Evaluate for Plasmodium parasites.
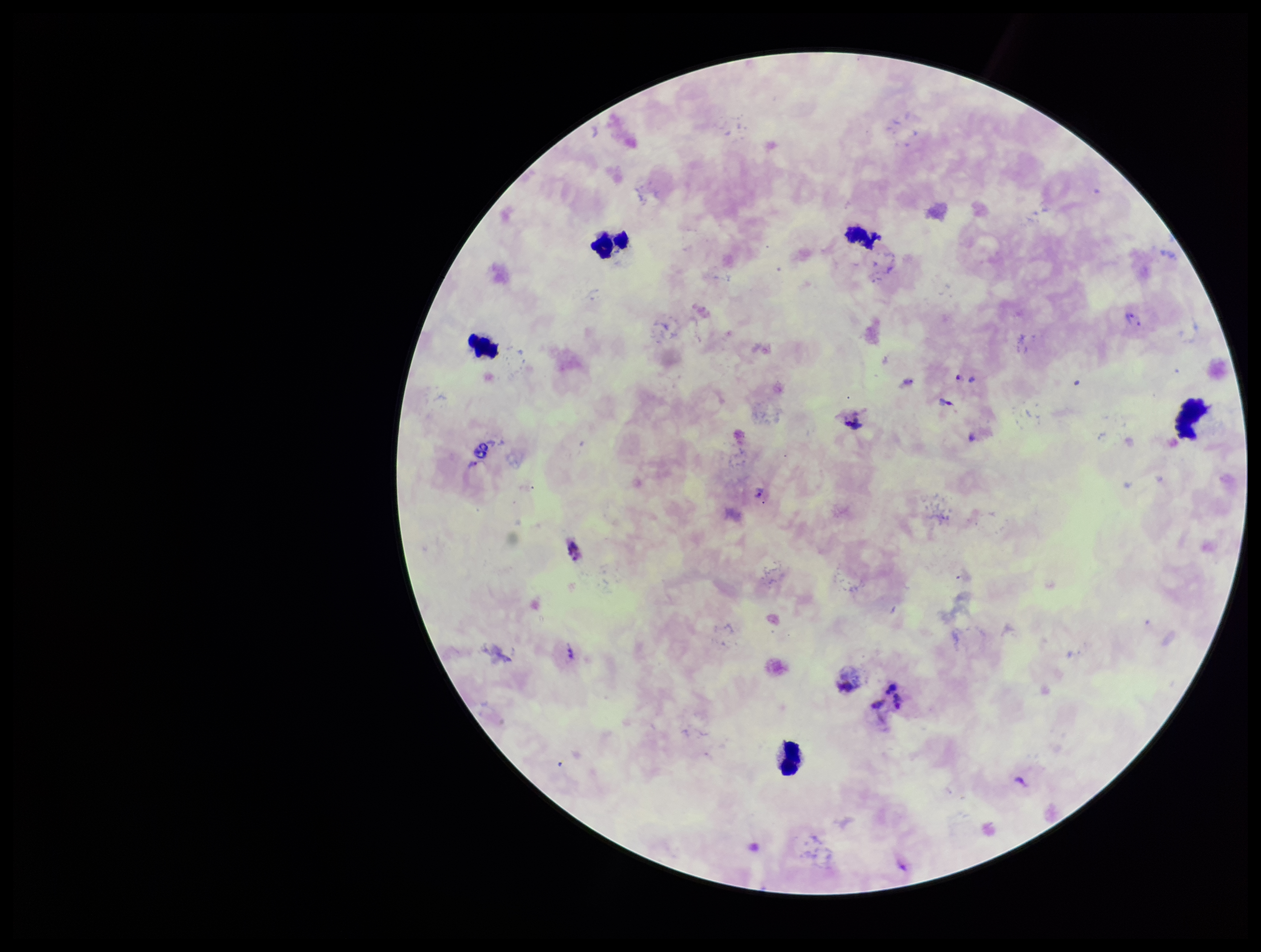

Identified.

{
  "capture": "smartphone photograph through the microscope eyepiece",
  "stain": "Giemsa",
  "species_reported_for_this_patient": "Plasmodium vivax",
  "patient_malaria_status": "infected",
  "field_of_view": "single",
  "parasite_count": 2,
  "leukocyte_count": 5,
  "preparation": "thick",
  "image_size": "1261×952 pixels"
}